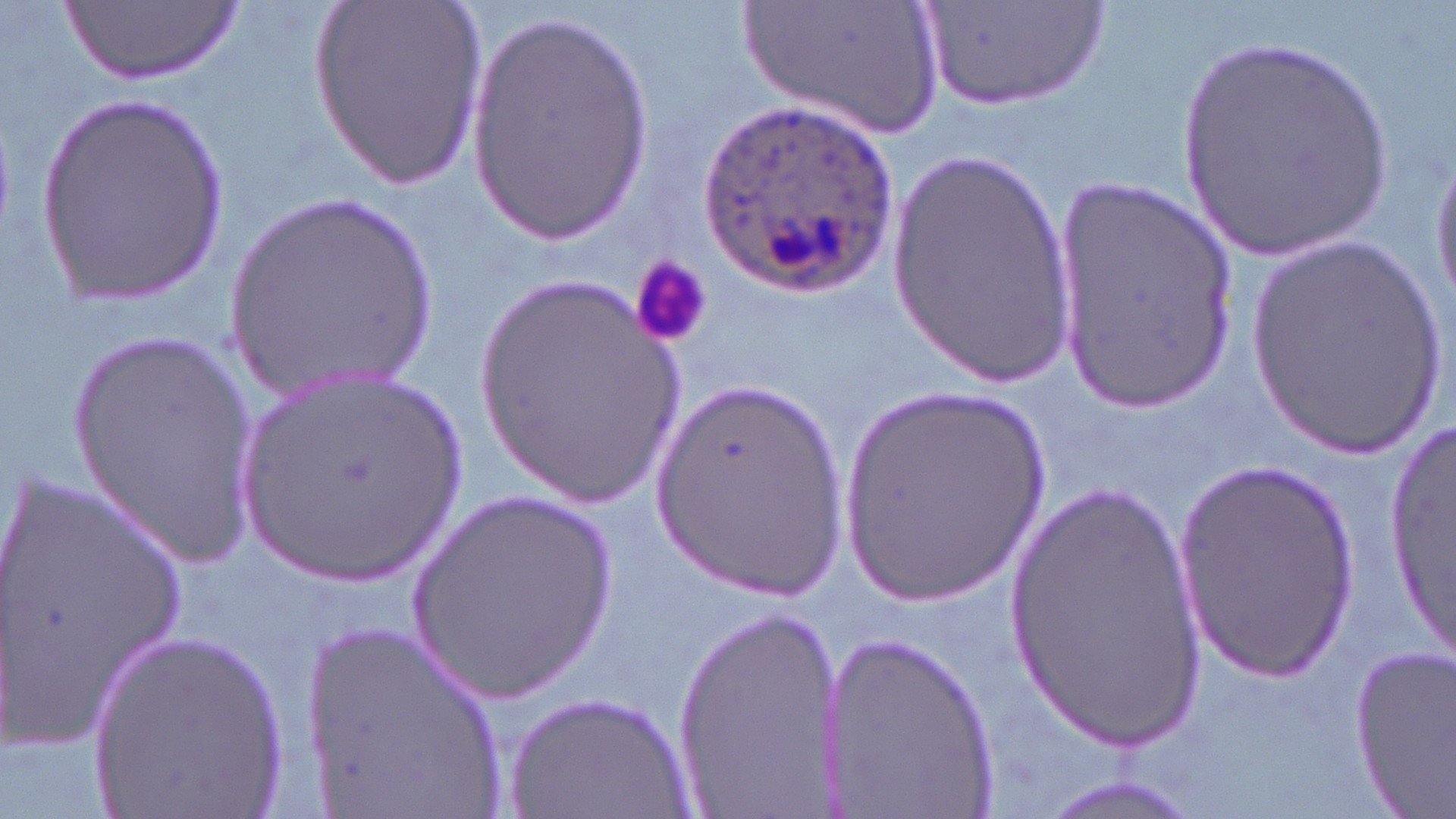 Approximate bounding boxes as (x1, y1, x2, y2) in pixels. Platelet locations: (630, 259, 713, 351). Uninfected red blood cell locations: (63, 0, 240, 86), (307, 0, 487, 188), (740, 0, 946, 138), (923, 0, 1107, 116), (464, 10, 658, 245), (1175, 31, 1402, 261), (34, 92, 230, 312), (1428, 137, 1456, 319), (880, 150, 1078, 386), (1054, 175, 1242, 408), (223, 191, 449, 402), (1242, 236, 1449, 457), (465, 270, 695, 508), (61, 327, 262, 563), (230, 372, 473, 591), (833, 377, 1058, 614), (649, 379, 850, 596), (1389, 399, 1453, 669), (1175, 458, 1362, 676), (4, 469, 190, 750), (1005, 473, 1209, 752), (407, 488, 623, 705), (673, 603, 841, 806), (300, 609, 516, 819), (89, 625, 296, 819), (828, 630, 1002, 817), (1348, 645, 1456, 813), (502, 691, 698, 817), (1031, 774, 1204, 819). Plasmodium ovale-infected red blood cell locations: (696, 98, 897, 296). Slide-level diagnosis: Plasmodium ovale. Single field of view. Thin blood film. Light microscopy. 1000x magnification. May-Grünwald-Giemsa stain. Image is 1456×819 pixels.